Classify this cell by malaria status.
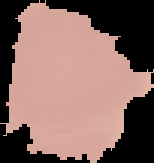

Uninfected.

Summary:
  - Preparation: thin blood smear
  - Image size: 154×163 pixels
  - Image type: segmented cell region on a black background